Locate every uninfected red blood cell.
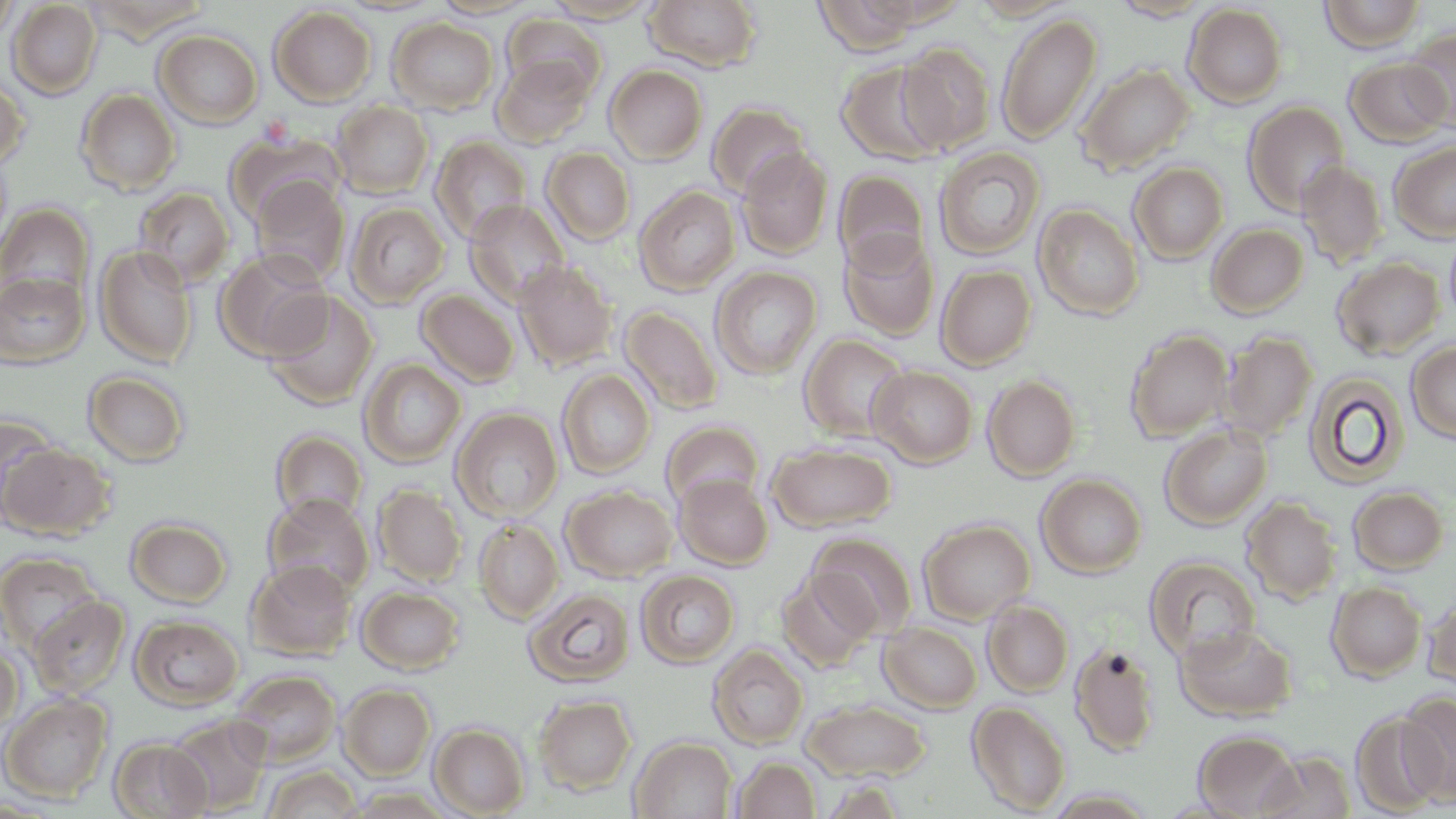
Approximate bounding boxes as (x1, y1, x2, y2) in pixels.
Uninfected red blood cells: (544, 0, 661, 23), (643, 0, 764, 72), (814, 0, 926, 55), (970, 0, 1076, 21), (1318, 0, 1426, 52), (0, 1, 19, 47), (7, 1, 102, 99), (430, 1, 538, 19), (1109, 1, 1215, 21), (1183, 3, 1288, 109), (269, 5, 377, 106), (997, 11, 1101, 144), (503, 14, 606, 102), (387, 17, 499, 114), (1401, 28, 1456, 131), (154, 30, 263, 128), (898, 41, 997, 154), (491, 55, 596, 148), (1344, 57, 1452, 147), (836, 61, 948, 166), (1077, 63, 1195, 174), (605, 65, 708, 164), (0, 75, 29, 170), (76, 88, 181, 195), (1242, 100, 1350, 216), (332, 101, 434, 198), (707, 101, 812, 199), (225, 131, 346, 226), (430, 136, 532, 244), (1389, 140, 1456, 243), (736, 146, 833, 260), (541, 147, 636, 246), (933, 147, 1045, 260), (1296, 161, 1388, 268), (1128, 162, 1228, 263), (833, 169, 930, 274), (249, 176, 351, 285), (133, 186, 235, 288), (635, 186, 740, 295), (465, 200, 570, 307), (345, 201, 449, 307), (0, 202, 95, 305), (1033, 203, 1144, 320), (1206, 223, 1309, 318), (1444, 225, 1456, 331), (839, 231, 940, 341), (94, 245, 199, 367), (214, 250, 331, 361), (1332, 257, 1445, 359), (514, 260, 618, 371), (936, 264, 1036, 369), (711, 266, 822, 380), (0, 271, 89, 367), (416, 289, 520, 387), (263, 291, 379, 409), (620, 305, 723, 415), (1124, 329, 1234, 442), (1219, 331, 1317, 440), (799, 333, 911, 443), (1406, 341, 1456, 444), (359, 358, 466, 468), (868, 366, 978, 467), (557, 369, 656, 478), (1303, 370, 1409, 489), (83, 371, 190, 467), (983, 374, 1080, 481), (451, 407, 563, 522), (0, 412, 64, 523), (661, 420, 764, 509), (1159, 424, 1272, 529), (270, 429, 368, 524), (767, 442, 897, 532), (1, 443, 115, 541), (674, 474, 773, 569), (1037, 474, 1147, 578), (373, 484, 466, 585), (561, 485, 678, 582), (1348, 486, 1449, 574), (264, 494, 374, 598), (1241, 495, 1342, 604), (126, 517, 232, 607), (474, 518, 563, 623), (918, 518, 1035, 624), (809, 532, 918, 639), (0, 551, 102, 652), (1144, 555, 1261, 663), (246, 559, 357, 661), (778, 566, 879, 671), (636, 569, 739, 667), (1327, 581, 1426, 681), (356, 586, 465, 674), (523, 587, 634, 687), (1423, 594, 1456, 690), (28, 595, 130, 699), (982, 599, 1074, 697), (130, 614, 244, 710), (879, 622, 982, 712), (1175, 624, 1298, 722), (1069, 641, 1160, 758), (0, 643, 23, 734), (707, 644, 808, 749), (231, 669, 341, 766), (339, 683, 435, 779), (1396, 692, 1455, 806), (0, 693, 114, 803), (534, 694, 637, 794), (802, 700, 931, 781), (967, 700, 1071, 816), (1352, 709, 1446, 814), (166, 714, 272, 814), (430, 723, 529, 817), (1193, 730, 1302, 818), (108, 737, 212, 818), (630, 737, 737, 818), (1255, 751, 1356, 818), (731, 757, 821, 818), (262, 764, 362, 818), (817, 779, 908, 818), (1045, 788, 1158, 818).

Slide-level diagnosis: no evidence of blood parasites. Thin blood film. One field of a larger specimen. Image is 1456×819 pixels. 1000x magnification. May-Grünwald-Giemsa-stained preparation. Light microscopy.